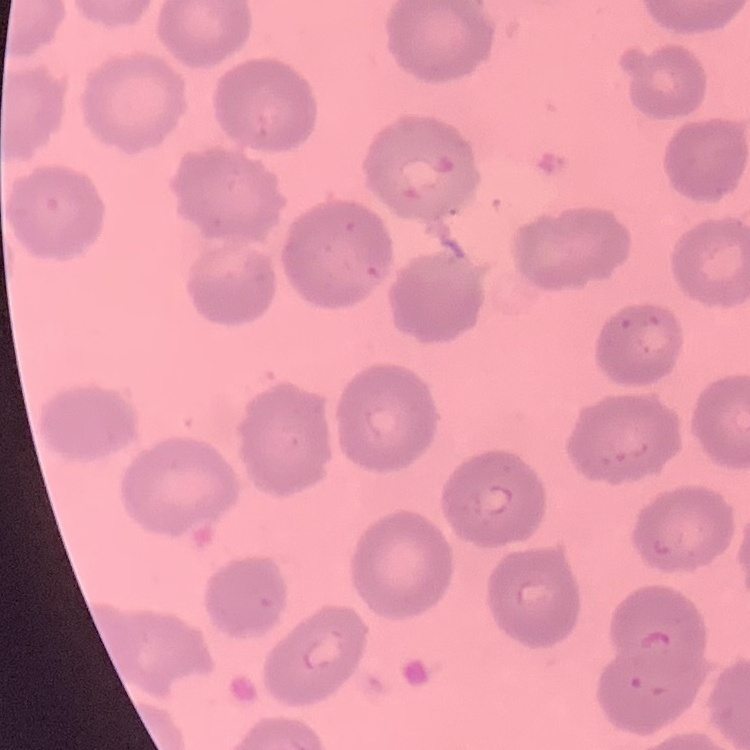

{
  "red_blood_cell_morphology": "no rouleaux formation",
  "preparation": "thin peripheral smear",
  "image_type": "one tile cut from a larger photomicrograph",
  "stain": "Field's or Giemsa"
}